Draw a bounding box around every malaria parasite, every leukocyte, and every artifact (stain precipitate or debris).
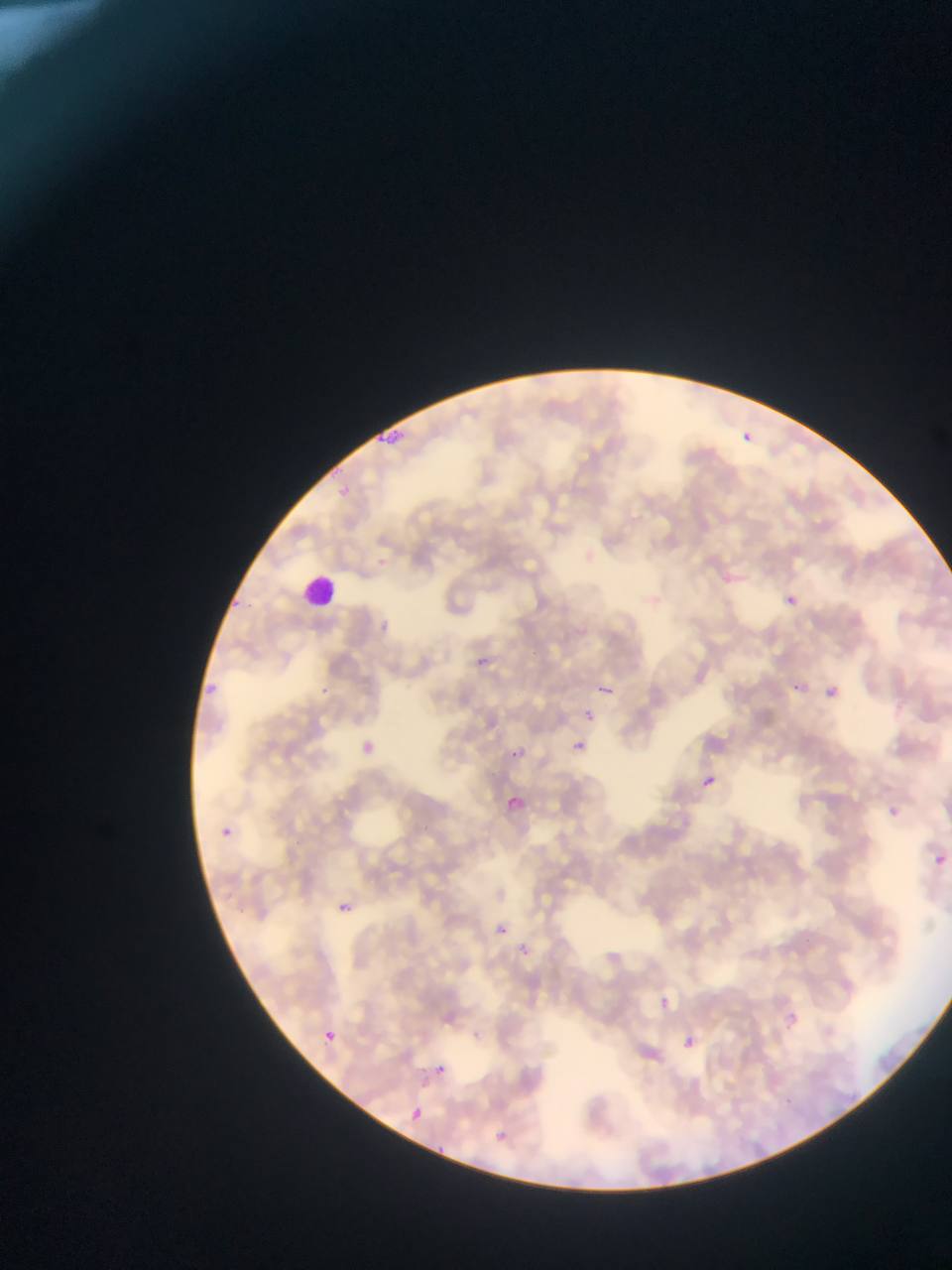

Approximate bounding boxes as left top right bottom in pixels.
Malaria parasites: 375 424 409 445; 742 430 754 443; 327 482 352 498; 718 571 735 586; 223 594 247 618; 784 594 799 607; 379 613 399 636; 481 655 494 672; 202 679 219 697; 604 679 629 719; 317 680 340 700; 793 683 805 693; 826 686 838 698; 577 706 602 720; 352 731 376 752; 567 737 590 754; 508 740 531 753; 703 776 716 789; 501 795 536 812; 222 819 236 843; 935 855 946 865; 339 903 352 913; 492 920 505 937; 653 993 676 1016; 783 1011 800 1029; 680 1027 700 1050; 325 1031 336 1041; 434 1064 446 1075; 408 1105 426 1124; 492 1128 522 1144.
Leukocytes: 300 576 337 611.

{
  "image_size": "952×1270 pixels",
  "preparation": "thin blood film",
  "field_of_view": "single",
  "country": "Ghana",
  "capture": "mobile-phone photograph through a microscope"
}